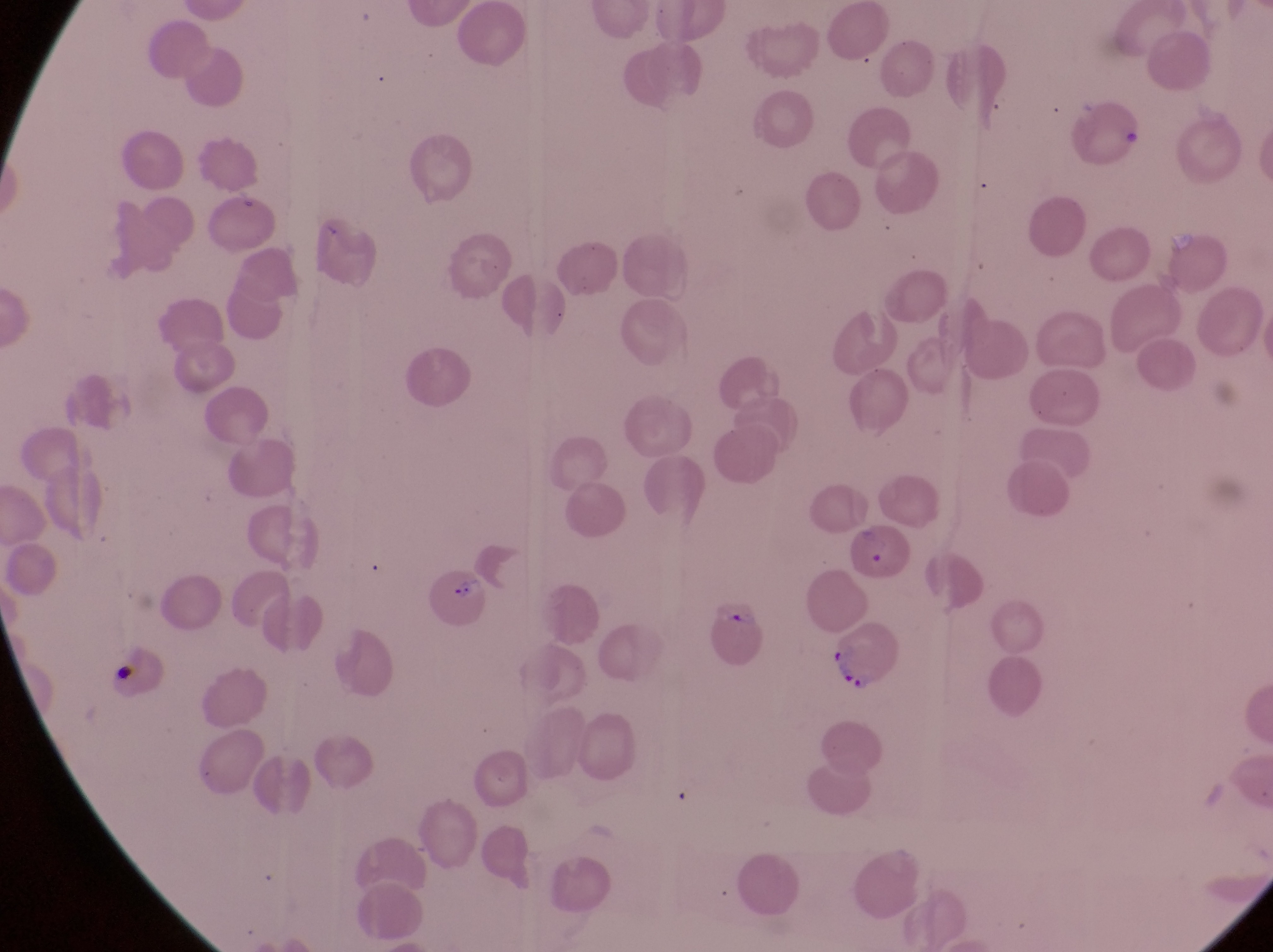

Approximate bounding boxes as [left, top, right, bottom] in pixels.
Summary:
  - Artifact (platelet-like body, stain precipitate, or debris) locations: [108, 645, 166, 706], [108, 667, 140, 687]
  - Parasitised red blood cell locations: [850, 525, 912, 580], [432, 575, 499, 637], [709, 592, 772, 674], [822, 619, 914, 699]
  - Magnification: 1000x
  - Capture: smartphone photograph through the eyepiece of an Olympus CX-23 microscope
  - Image size: 1273×952 pixels
  - Field of view: single
  - Preparation: thin blood film
  - Country: Uganda